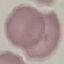
Summary:
  - Malaria status: uninfected
  - Image type: cell patch, automatically extracted from a larger field of view and resized to 64 × 64 pixels
  - Stain: Giemsa
  - Preparation: thin blood smear
  - Capture: smartphone through the microscope eyepiece